Give the position of every Plasmodium parasite.
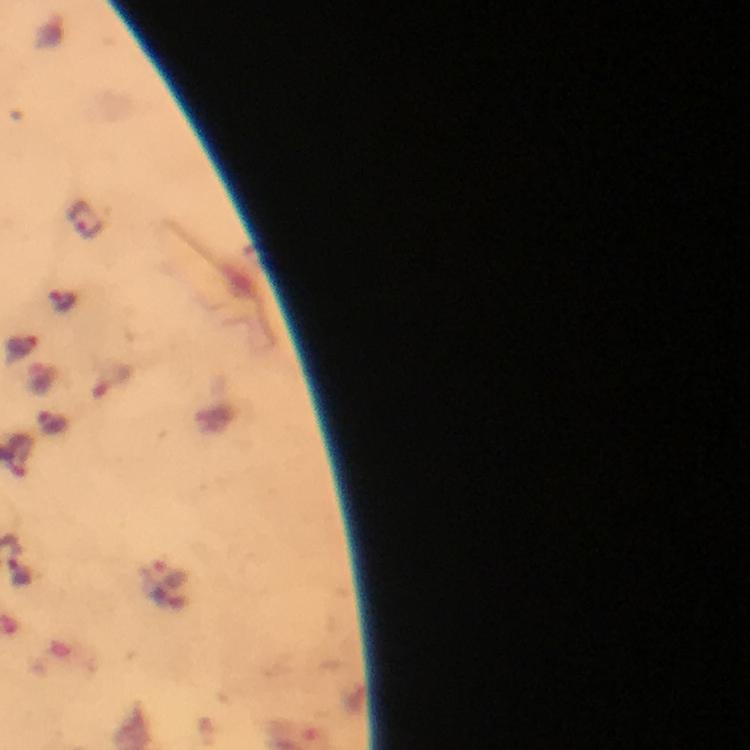

Approximate centers as (x, y) in pixels.
Plasmodium parasites: (85, 217), (62, 301), (20, 573).

Summary:
  - Preparation: thick blood film
  - Stain: Giemsa
  - Capture: smartphone mounted on the microscope
  - Immersion oil: used
  - Cropped from: one field of view
  - Magnification: 100x
  - Context: from a malaria diagnostic workup
  - Image size: 750×750 pixels